Identify the preparation type.
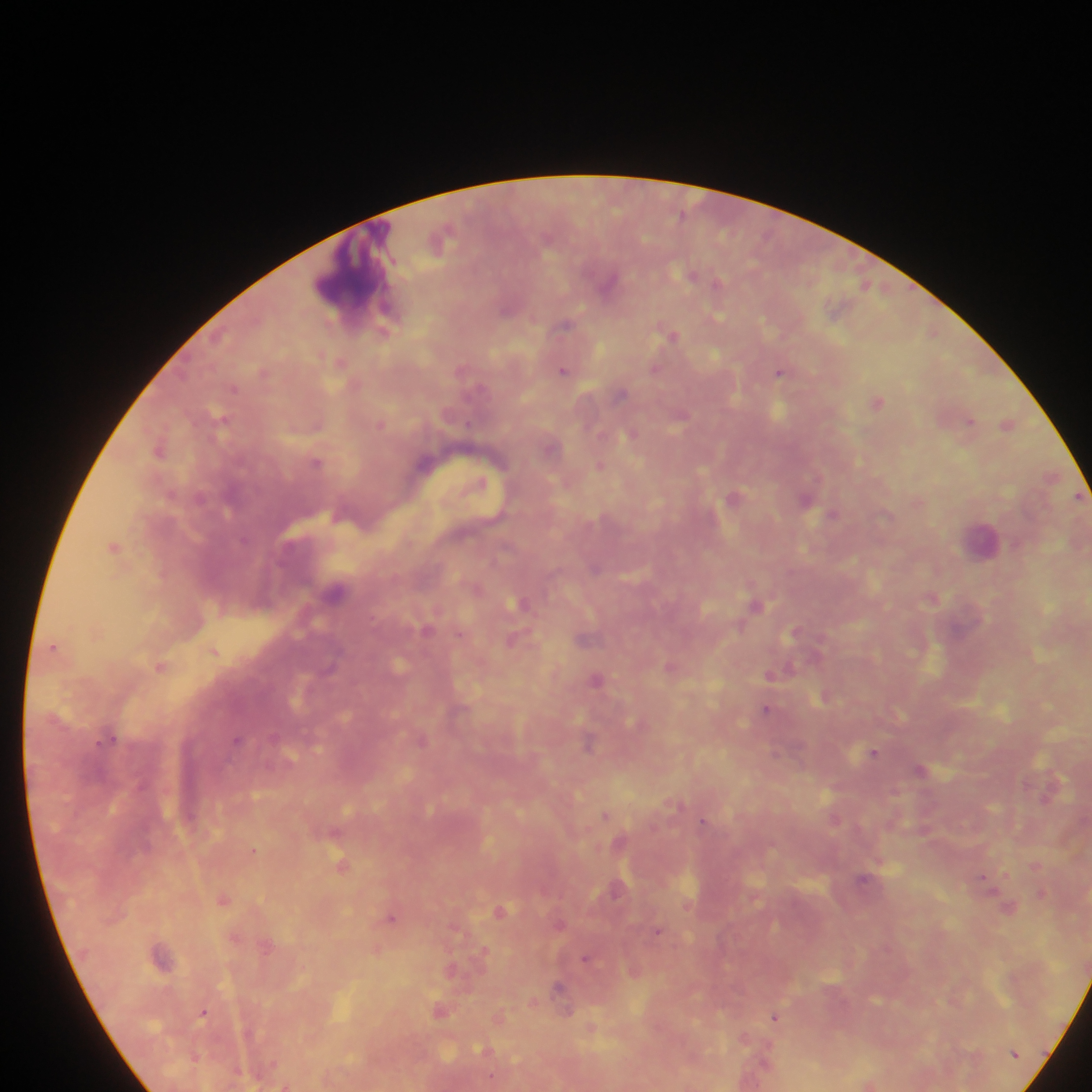

Thick blood film.

capture = mobile-phone photograph through a microscope
image size = 1092×1092 pixels
Plasmodium parasite locations = approximate centers as [x, y] in pixels: [691, 275], [609, 282], [718, 283], [507, 309], [387, 310], [717, 317], [566, 325], [671, 334], [654, 368], [563, 369], [779, 372], [234, 388], [620, 394], [878, 401], [970, 420], [1008, 423], [381, 424], [631, 434], [159, 450], [317, 461], [600, 465], [736, 496], [806, 501], [833, 515], [244, 540], [114, 547], [596, 568], [336, 591], [519, 602], [757, 605], [426, 629], [795, 632], [512, 640], [214, 651], [160, 666], [772, 674], [598, 679], [766, 709], [110, 737], [237, 739], [422, 739], [589, 742], [873, 752], [775, 753], [920, 769], [676, 804], [605, 816], [703, 820], [253, 851], [341, 865], [982, 877], [863, 879], [617, 889], [1041, 894], [223, 900], [1008, 908], [501, 910], [391, 918], [560, 923], [657, 931], [482, 952], [586, 958], [558, 987], [439, 1010], [203, 1013], [775, 1017], [196, 1057], [285, 1086]
leukocyte locations = approximate centers as [x, y] in pixels: [353, 269], [981, 539]
field of view = single
country = Ghana